State the preparation type.
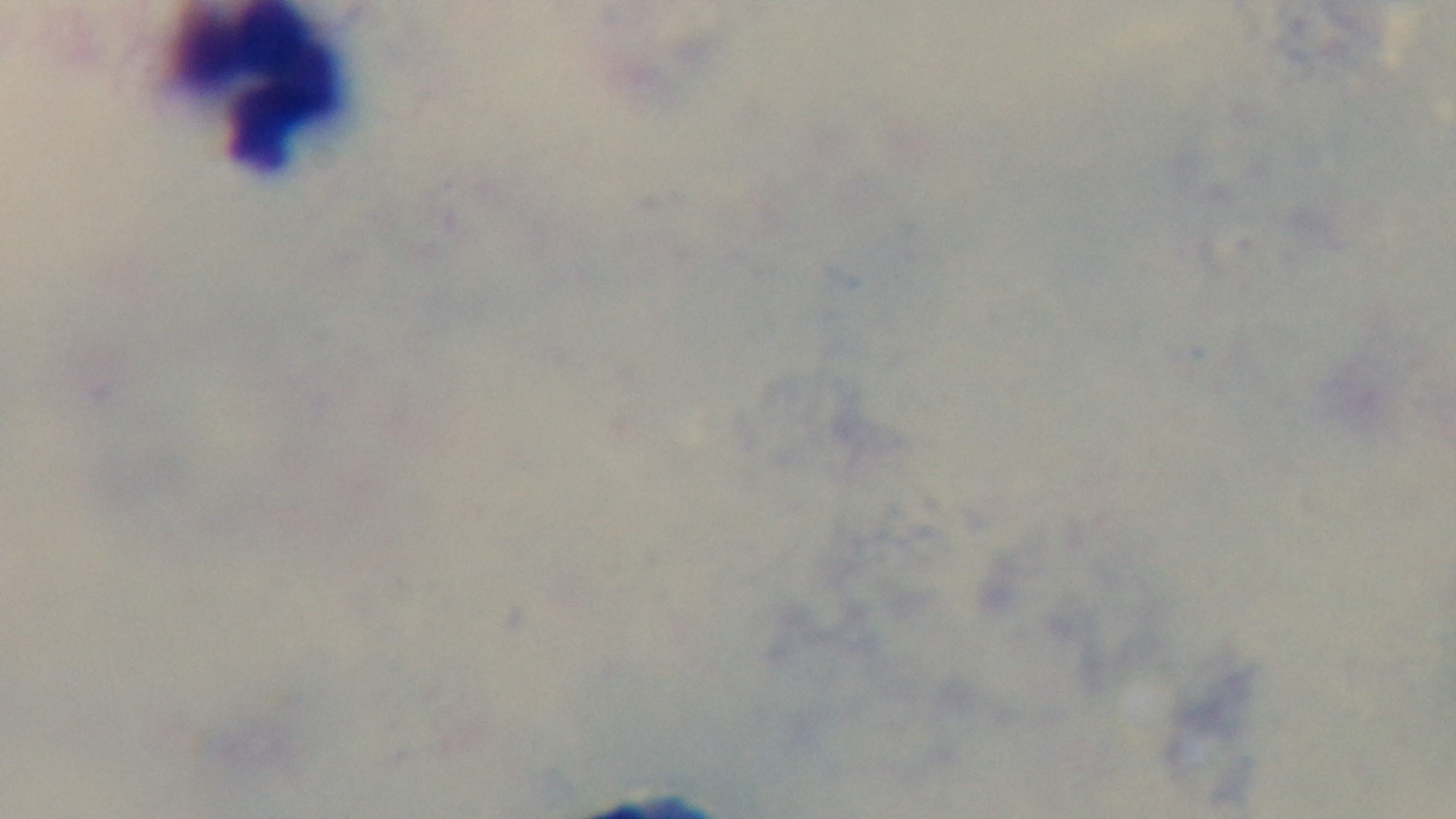
Thick.

Malaria status: uninfected. One field from the slide. Mounted 4K digital camera. Giemsa-stained. Photomicrograph. Oil-immersion objective, 100x.